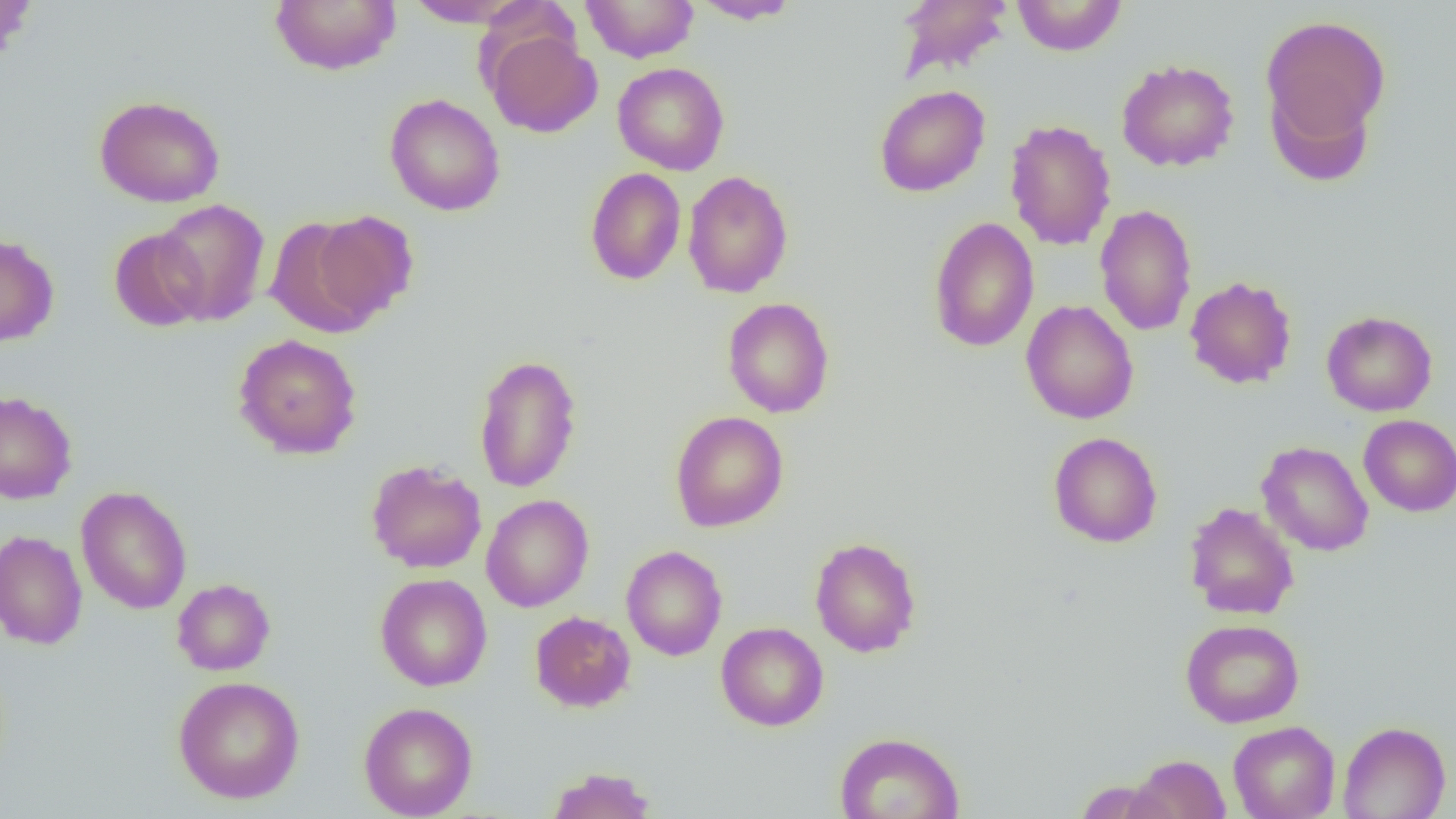
slide-level diagnosis = negative for blood parasites
modality = light microscopy
field of view = one of a larger specimen
preparation = thin blood film
magnification = 1000x
uninfected red blood cell locations = approximate bounding boxes as [x1, y1, x2, y2] in pixels: [0, 0, 37, 68], [270, 0, 401, 75], [691, 0, 801, 24], [894, 0, 1014, 83], [1011, 0, 1127, 56], [404, 1, 528, 27], [581, 1, 698, 63], [1260, 14, 1392, 154], [483, 26, 602, 138], [1116, 58, 1240, 172], [613, 62, 729, 175], [1265, 80, 1377, 188], [874, 85, 990, 197], [384, 93, 506, 216], [94, 95, 226, 207], [1004, 119, 1117, 251], [585, 167, 686, 285], [682, 170, 794, 298], [154, 199, 271, 326], [1095, 204, 1198, 336], [309, 211, 419, 325], [266, 215, 381, 337], [928, 216, 1040, 353], [109, 227, 210, 332], [0, 233, 59, 346], [1185, 275, 1297, 389], [721, 297, 835, 418], [1021, 300, 1139, 424], [1321, 310, 1437, 416], [232, 333, 363, 459], [472, 354, 583, 493], [0, 390, 77, 504], [669, 411, 788, 532], [1358, 414, 1456, 516], [1048, 431, 1163, 548], [1257, 441, 1374, 557], [365, 459, 487, 574], [76, 486, 192, 614], [481, 494, 594, 612], [1183, 501, 1299, 620], [0, 529, 87, 650], [809, 536, 922, 657], [621, 545, 727, 661], [375, 573, 492, 691], [172, 578, 275, 676], [530, 611, 635, 712], [1180, 619, 1305, 728], [716, 621, 829, 731], [173, 675, 305, 804], [358, 701, 477, 819], [1227, 720, 1340, 819], [1338, 721, 1451, 819], [834, 731, 965, 819], [1127, 754, 1232, 818], [544, 766, 657, 818], [1072, 778, 1177, 819]
image size = 1456×819 pixels